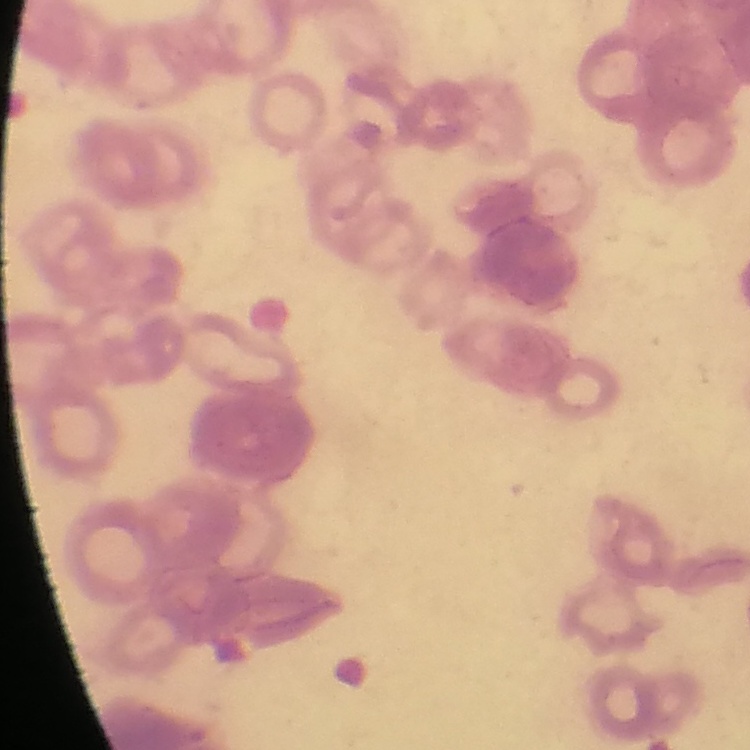
Summary:
  - Red blood cell morphology: rouleaux formation
  - Stain: Field's or Giemsa
  - Image type: square crop of a larger photomicrograph
  - Preparation: thin peripheral smear